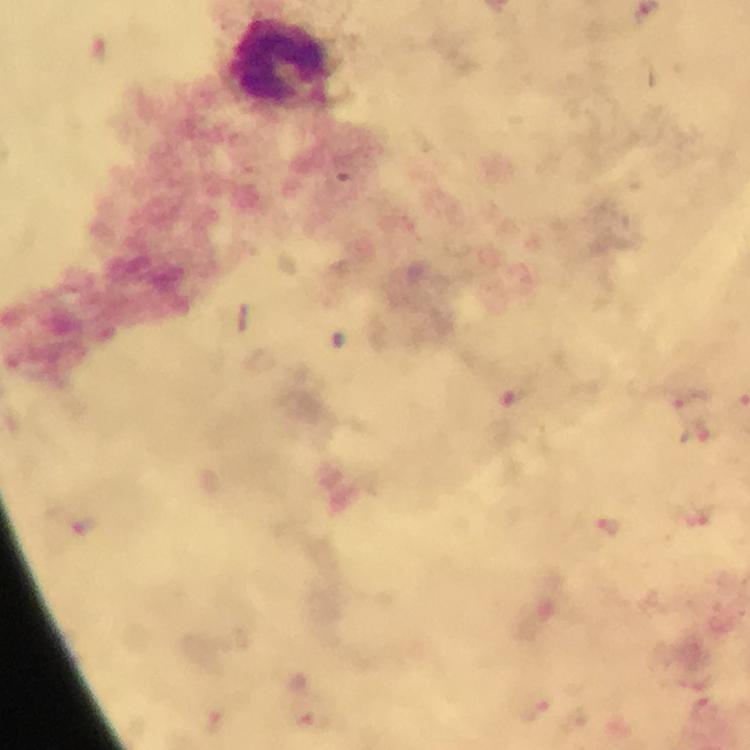

Approximate centers as (x, y) in pixels.
Summary:
  - Leukocyte locations: (280, 60)
  - Context: from a diagnostic examination for malaria
  - Image size: 750×750 pixels
  - Magnification: 100x
  - Malaria parasites: none detected
  - Capture: smartphone camera through the microscope
  - Cropped from: one field of view
  - Immersion oil: applied
  - Preparation: thick smear
  - Stain: Giemsa